Describe the morphology of the erythrocytes.
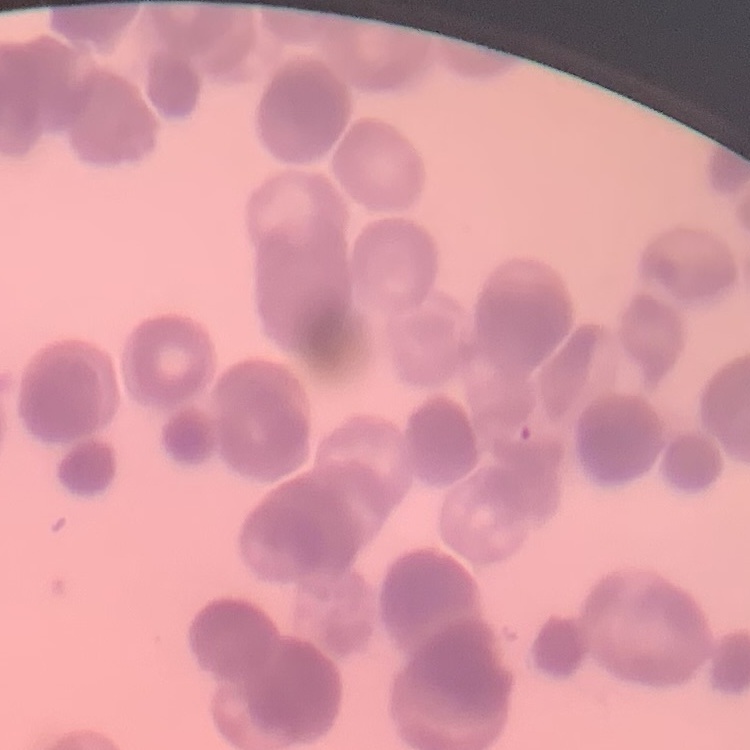

Rouleaux formation.

stain = Field's or Giemsa
preparation = thin blood smear
image type = one tile cut from a larger photomicrograph